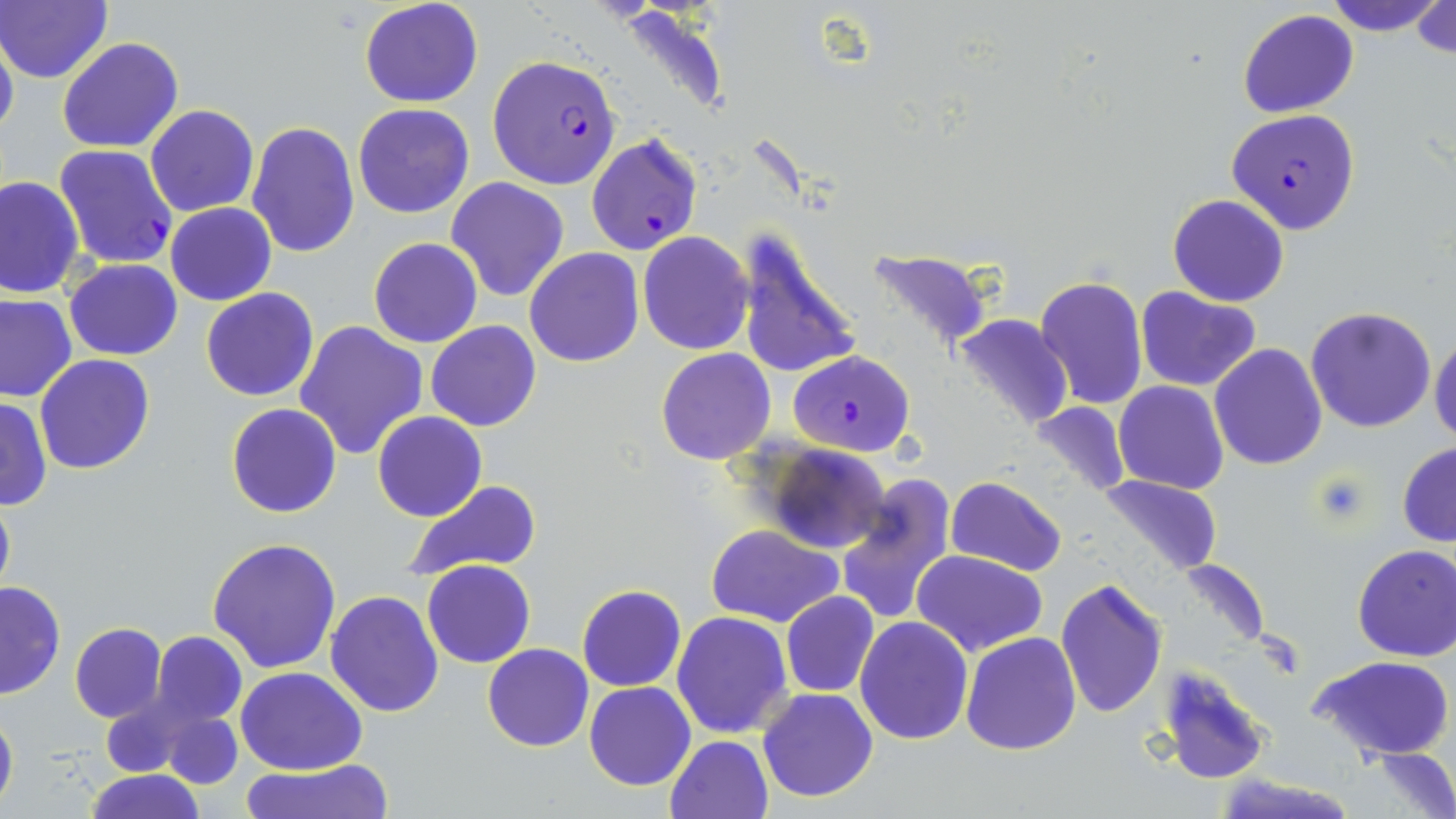
slide-level diagnosis = Plasmodium falciparum
field of view = single
preparation = thin blood film
modality = optical microscopy
uninfected red blood cell locations = approximate bounding boxes as (x1,y1)-(x2,y2) corner pairs in pixels: (359,0)-(483,108), (1325,0)-(1446,35), (1412,0)-(1455,58), (0,1)-(113,85), (1237,8)-(1359,118), (0,30)-(18,145), (56,37)-(184,153), (352,102)-(475,218), (145,104)-(260,217), (245,120)-(361,256), (0,175)-(85,297), (445,177)-(569,302), (1168,194)-(1290,307), (166,203)-(276,306), (729,230)-(863,383), (639,231)-(753,354), (368,238)-(482,349), (525,247)-(644,366), (865,249)-(995,353), (64,258)-(182,360), (1034,274)-(1147,411), (1135,287)-(1261,391), (200,288)-(319,402), (0,293)-(77,403), (215,298)-(392,433), (1305,306)-(1436,432), (953,314)-(1074,432), (293,320)-(429,460), (426,321)-(542,433), (1429,332)-(1456,443), (1209,343)-(1327,469), (656,348)-(775,465), (35,354)-(157,474), (1114,381)-(1230,495), (0,398)-(50,511), (1032,402)-(1132,499), (226,403)-(342,519), (372,412)-(488,522), (1396,442)-(1456,547), (762,443)-(886,554), (836,474)-(959,627), (945,474)-(1067,576), (1098,474)-(1223,575), (401,478)-(544,581), (0,485)-(15,606), (705,524)-(844,629), (209,536)-(342,672), (1352,544)-(1456,661), (911,550)-(1049,658), (1178,558)-(1271,651), (421,560)-(534,668), (1055,578)-(1169,718), (0,581)-(65,699), (577,585)-(686,691), (325,589)-(446,717), (781,591)-(879,697), (672,610)-(793,739), (855,616)-(973,743), (69,622)-(167,722), (150,630)-(248,729), (960,630)-(1081,754), (482,643)-(593,751), (1310,654)-(1455,765), (1158,664)-(1269,785), (236,667)-(367,776), (584,681)-(696,792), (757,688)-(879,802), (0,705)-(18,813), (159,707)-(242,790), (665,735)-(774,819), (1363,749)-(1456,819), (238,760)-(397,818), (85,771)-(206,819), (1214,774)-(1361,819)
stain = May-Grünwald-Giemsa
Plasmodium falciparum-infected red blood cell locations = approximate bounding boxes as (x1,y1)-(x2,y2) corner pairs in pixels: (487,54)-(622,190), (1229,108)-(1360,235), (586,134)-(702,255), (54,144)-(179,268), (788,350)-(916,457)
magnification = 1000x
image size = 1456×819 pixels